Draw a bounding box around every leukocyte (white blood cell).
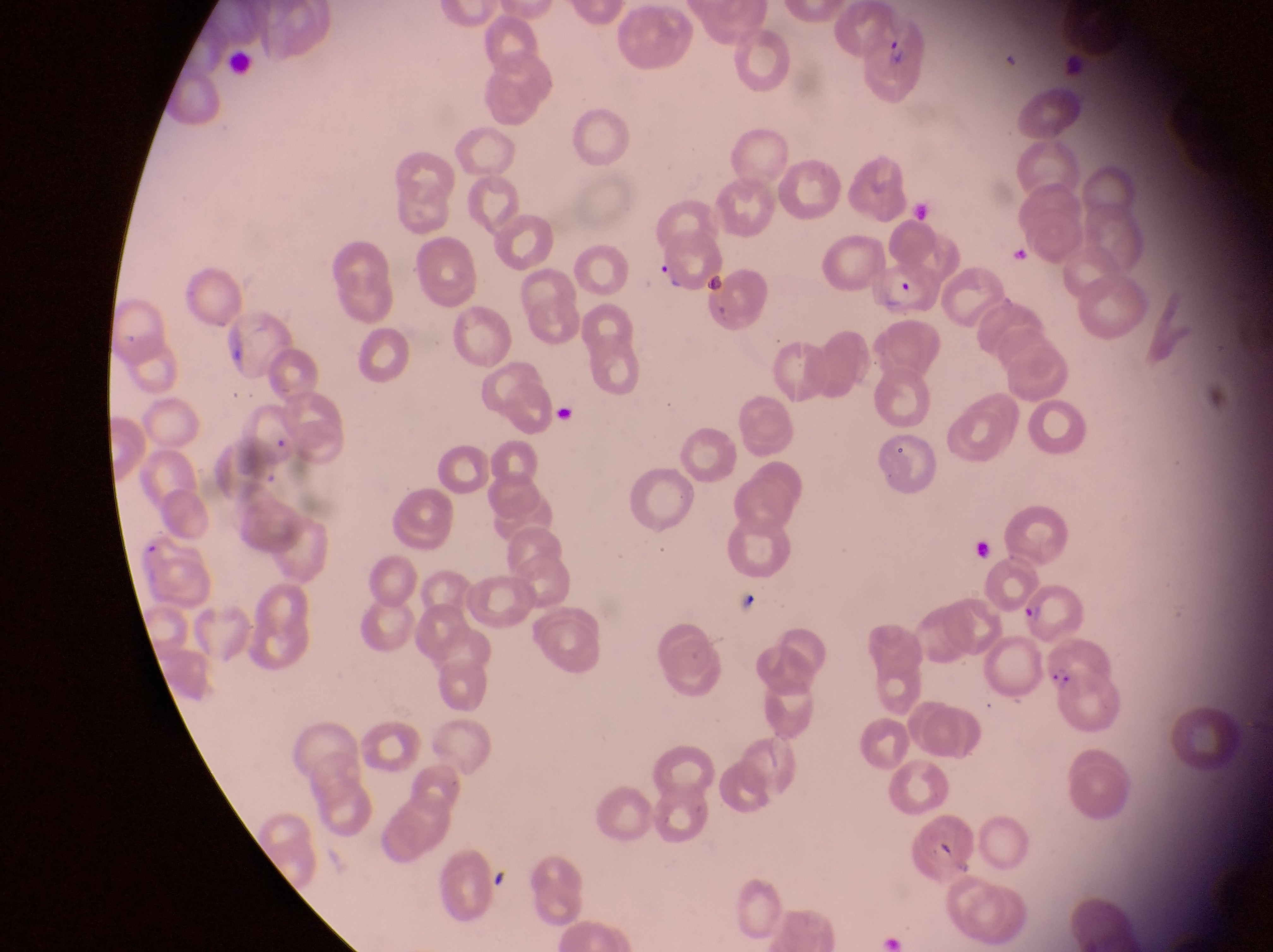

No leukocytes observed.

Approximate bounding boxes as {left, top, right, bottom} in pixels.
Summary:
  - Parasitised red blood cell locations: {861, 13, 927, 103}, {876, 264, 958, 324}, {1019, 580, 1091, 647}, {1045, 646, 1119, 732}
  - Country: Uganda
  - Image size: 1273×952 pixels
  - Magnification: 1000x
  - Field of view: single
  - Preparation: thin blood film
  - Capture: smartphone photograph through the eyepiece of an Olympus CX-23 microscope